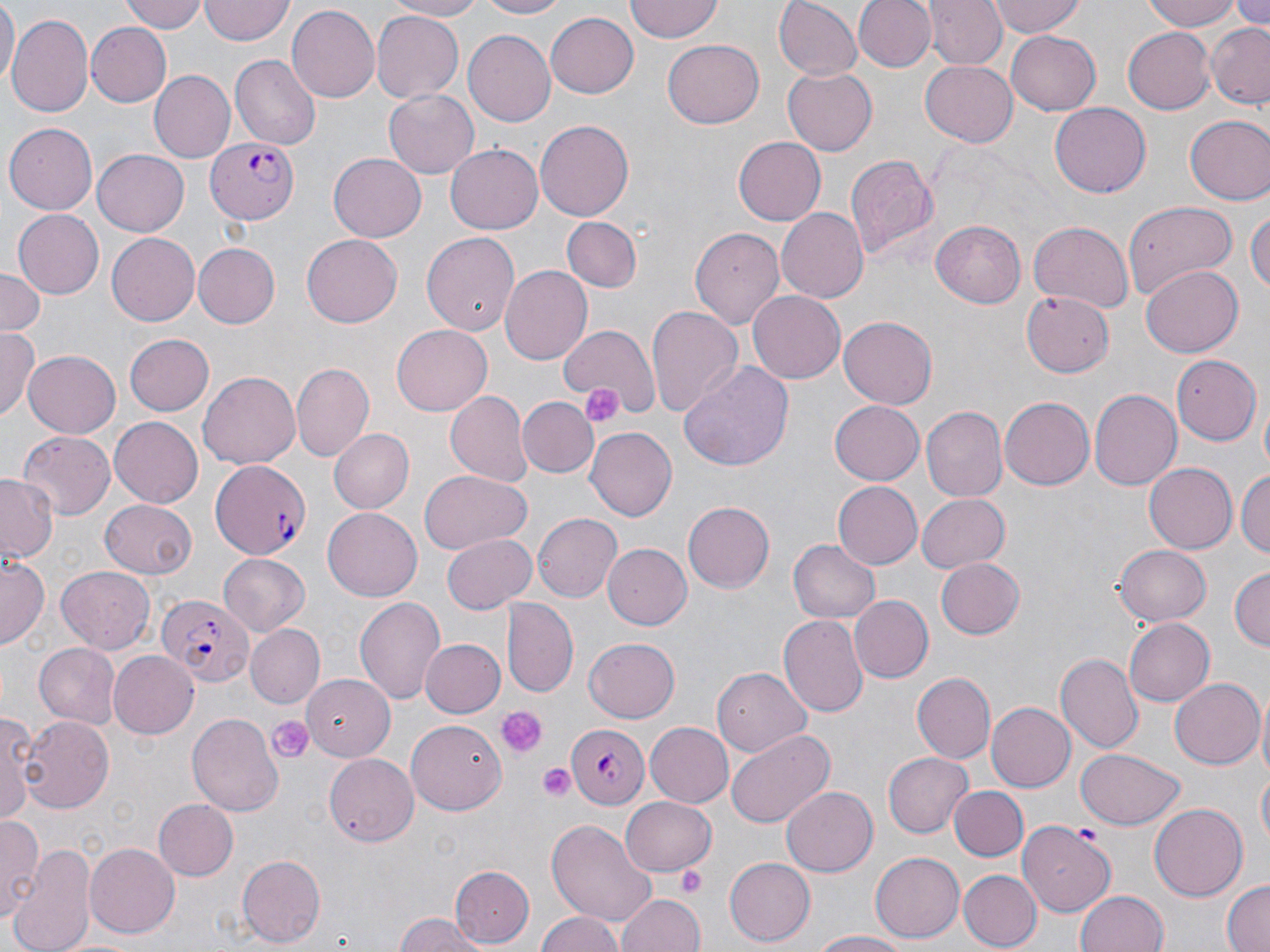 Approximate bounding boxes as [x1, y1, x2, y2] in pixels. Platelet locations: [578, 380, 625, 426], [496, 705, 544, 757], [267, 717, 314, 763], [538, 762, 578, 803], [677, 868, 705, 896]. Plasmodium falciparum-infected red blood cell locations: [206, 134, 299, 224], [209, 457, 312, 560], [158, 591, 254, 687], [567, 725, 654, 805]. Uninfected red blood cell locations: [0, 0, 17, 92], [120, 0, 209, 33], [382, 0, 492, 20], [473, 0, 569, 19], [772, 0, 862, 80], [854, 0, 936, 74], [991, 0, 1085, 39], [1143, 0, 1250, 29], [1228, 0, 1270, 34], [199, 1, 294, 45], [624, 1, 728, 43], [927, 1, 1005, 70], [288, 4, 380, 104], [546, 11, 638, 98], [371, 12, 462, 102], [8, 15, 94, 115], [87, 23, 170, 105], [1205, 24, 1269, 108], [1122, 26, 1216, 113], [465, 29, 555, 124], [1005, 30, 1102, 115], [663, 37, 765, 129], [231, 55, 320, 149], [920, 57, 1020, 146], [783, 67, 877, 157], [150, 70, 234, 162], [384, 90, 479, 179], [1050, 101, 1151, 197], [1185, 114, 1270, 205], [535, 119, 633, 222], [5, 123, 98, 212], [734, 135, 829, 226], [446, 144, 544, 235], [93, 152, 187, 236], [328, 152, 427, 241], [844, 152, 940, 264], [1123, 200, 1235, 302], [1248, 204, 1269, 304], [11, 207, 103, 296], [776, 207, 867, 302], [562, 216, 643, 291], [931, 220, 1025, 308], [1029, 221, 1134, 313], [689, 225, 784, 329], [422, 231, 520, 337], [105, 232, 199, 326], [301, 234, 403, 328], [193, 243, 280, 327], [500, 265, 592, 365], [1142, 266, 1244, 357], [0, 267, 45, 335], [1020, 288, 1116, 377], [748, 291, 846, 386], [644, 305, 743, 420], [838, 316, 938, 409], [558, 323, 657, 415], [390, 325, 492, 417], [0, 328, 38, 422], [125, 332, 214, 415], [22, 351, 120, 439], [1171, 353, 1261, 443], [678, 360, 794, 472], [292, 363, 374, 460], [198, 371, 300, 468], [1088, 389, 1181, 492], [444, 390, 530, 487], [519, 396, 597, 477], [999, 396, 1094, 491], [828, 400, 926, 487], [1258, 401, 1270, 474], [920, 405, 1007, 502], [109, 418, 203, 507], [328, 427, 414, 514], [585, 428, 676, 521], [15, 431, 116, 519], [1145, 462, 1237, 553], [419, 469, 532, 556], [1236, 469, 1270, 561], [0, 473, 56, 563], [833, 481, 922, 569], [915, 493, 1009, 574], [98, 499, 199, 579], [683, 501, 777, 593], [323, 505, 422, 598], [532, 512, 623, 602], [443, 535, 535, 613], [787, 538, 880, 625], [601, 544, 690, 631], [1113, 544, 1212, 625], [217, 553, 309, 637], [0, 554, 47, 651], [936, 557, 1024, 639], [56, 565, 157, 652], [1229, 567, 1269, 651], [851, 595, 932, 682], [354, 597, 446, 705], [503, 599, 577, 695], [778, 615, 868, 718], [1122, 617, 1214, 707], [249, 624, 327, 712], [583, 637, 681, 722], [422, 638, 505, 718], [33, 643, 118, 727], [106, 650, 200, 738], [1058, 653, 1143, 751], [712, 667, 812, 757], [303, 672, 395, 759], [914, 672, 994, 763], [1168, 677, 1264, 770], [1255, 699, 1270, 785], [986, 703, 1074, 790], [0, 708, 36, 826], [187, 712, 282, 814], [20, 715, 116, 810], [406, 719, 506, 812], [645, 722, 732, 805], [725, 728, 835, 829], [1076, 749, 1185, 830], [883, 752, 973, 836], [324, 753, 418, 846], [1257, 769, 1270, 847], [782, 785, 878, 877], [950, 787, 1027, 863], [619, 796, 717, 876], [152, 799, 238, 881], [1150, 803, 1247, 900], [0, 815, 43, 924], [545, 817, 657, 928], [1019, 821, 1117, 916], [7, 841, 96, 952], [84, 842, 181, 938], [869, 853, 965, 942], [236, 855, 325, 948], [723, 856, 814, 946], [451, 866, 535, 945], [958, 869, 1041, 951], [1220, 880, 1270, 952], [1076, 889, 1169, 952], [616, 890, 706, 952], [535, 909, 625, 952], [392, 914, 487, 952], [810, 930, 918, 951]. Slide-level diagnosis: Plasmodium falciparum. Light microscopy. One field of a larger specimen. Image is 1270×952 pixels. Captured at 1000x magnification. Thin blood film. May-Grünwald-Giemsa stain.